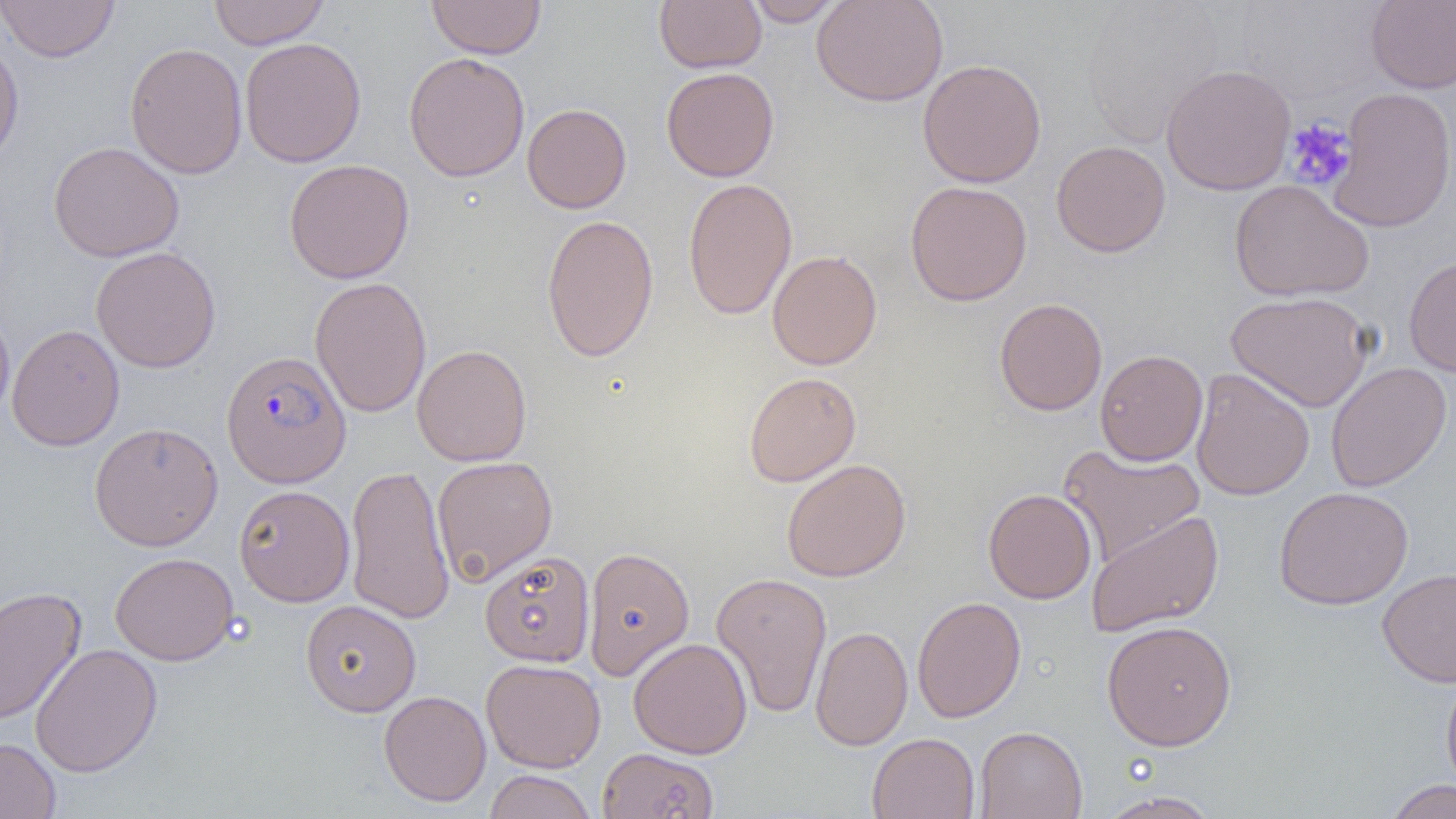
Summary:
  - Coordinate format: approximate bounding boxes as (x1,y1)-(x2,y2) corner pairs in pixels
  - Plasmodium falciparum-infected red blood cell locations: (221,350)-(351,488)
  - Platelet locations: (1284,117)-(1356,191)
  - Uninfected red blood cell locations: (208,0)-(329,49), (654,0)-(766,73), (743,0)-(845,26), (811,0)-(948,107), (0,1)-(120,62), (427,1)-(545,59), (1365,1)-(1456,93), (1078,2)-(1227,147), (0,36)-(24,166), (240,37)-(366,167), (125,42)-(247,179), (403,51)-(530,182), (917,58)-(1046,188), (1160,63)-(1296,196), (661,67)-(780,182), (1329,87)-(1456,232), (522,103)-(631,214), (1051,140)-(1171,258), (48,141)-(184,262), (284,158)-(414,284), (683,178)-(797,320), (1229,179)-(1374,302), (904,181)-(1032,306), (541,213)-(659,362), (90,246)-(221,372), (767,249)-(882,370), (1403,255)-(1456,377), (309,277)-(431,417), (1226,291)-(1374,412), (994,297)-(1107,416), (0,308)-(14,424), (6,324)-(125,451), (412,344)-(532,467), (1094,349)-(1208,466), (1325,362)-(1452,492), (1191,368)-(1315,501), (743,371)-(861,487), (89,421)-(224,551), (1057,444)-(1205,568), (431,456)-(557,586), (782,458)-(911,582), (344,463)-(455,625), (234,484)-(355,606), (1274,486)-(1414,610), (983,488)-(1097,604), (1086,510)-(1225,637), (582,545)-(695,680), (479,551)-(595,667), (110,552)-(238,665), (1377,568)-(1456,687), (711,572)-(832,719), (0,586)-(86,726), (911,595)-(1027,723), (301,599)-(421,717), (1101,620)-(1237,751), (810,625)-(913,751), (628,637)-(753,759), (30,643)-(163,777), (481,658)-(606,772), (1441,671)-(1456,797), (379,690)-(491,806), (974,726)-(1088,819), (867,732)-(980,819), (0,737)-(61,819), (598,747)-(719,819), (483,770)-(597,819), (1382,779)-(1456,819), (1096,791)-(1223,818)
  - Slide-level diagnosis: Plasmodium falciparum
  - Image size: 1456×819 pixels
  - Magnification: 1000x
  - Preparation: thin blood film
  - Field of view: single
  - Modality: optical microscopy